Assess this cell for malaria.
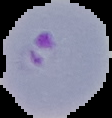

It is parasitized.

Summary:
  - Preparation: thin blood smear
  - Image size: 112×118 pixels
  - Image type: segmented cell region with the area outside set to black